Name the cell type shown.
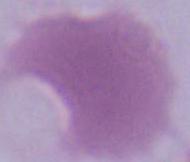

This is an erythrocyte.

Summary:
  - Magnification: 1000x
  - Modality: photomicrograph